Comment on the morphology of the erythrocytes.
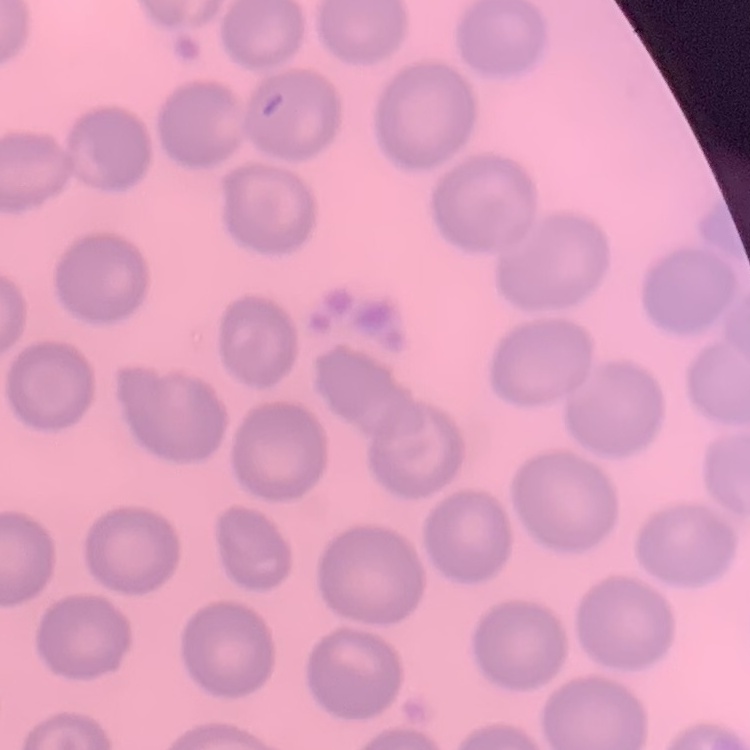

They show no rouleaux formation.

One tile cut from a larger photomicrograph. Thin blood smear. Stained with either Field's or Giemsa.